Assess the morphology of the erythrocytes.
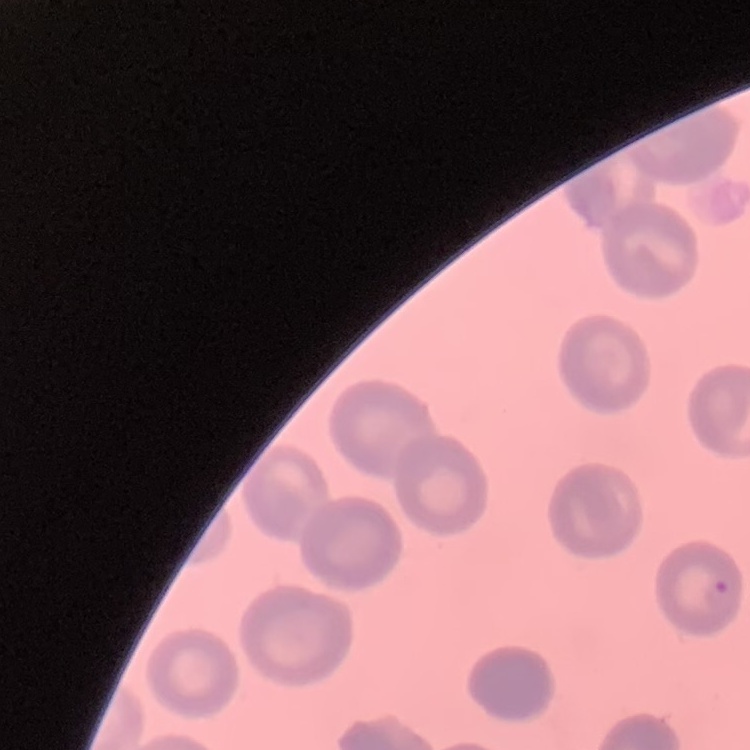

They show no rouleaux formation.

Field's or Giemsa stain. One tile cut from a larger photomicrograph. Thin peripheral smear.